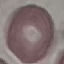

Malaria status: uninfected. Automatically extracted cell patch, resized to 64 × 64 pixels. Photographed with a smartphone camera at the microscope eyepiece. Thin blood smear. Giemsa stain.